Locate every blood parasite and identify its species.
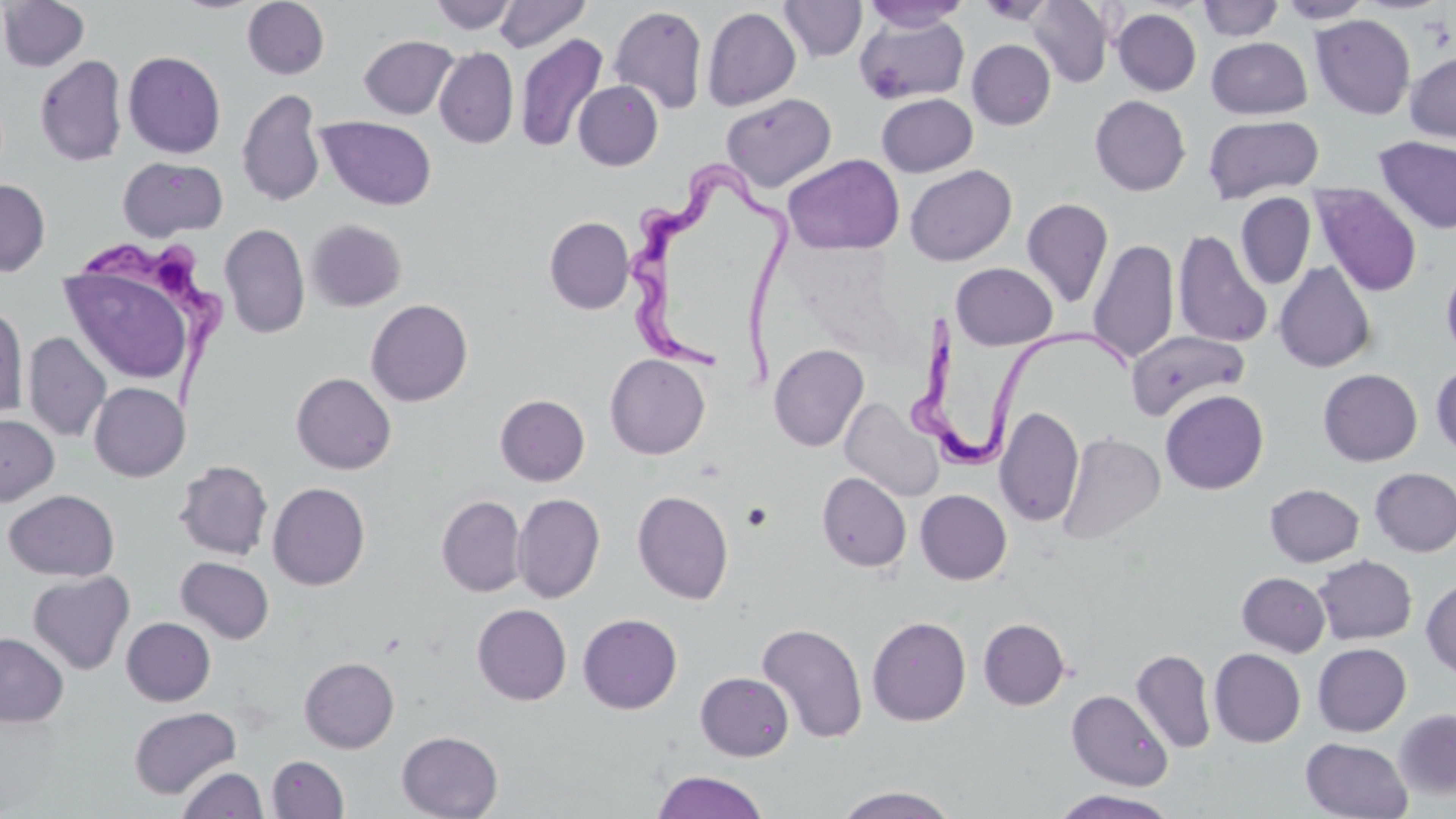
Approximate bounding boxes as (x1, y1, x2, y2) in pixels.
Trypanosoma brucei: (627, 163, 792, 391), (78, 238, 228, 414), (908, 308, 1136, 478).
No Plasmodium falciparum, Plasmodium ovale, Plasmodium malariae, Plasmodium vivax, or Babesia divergens observed.

Summary:
  - Uninfected red blood cell locations: (0, 0, 90, 72), (242, 0, 329, 79), (428, 0, 518, 35), (493, 0, 592, 52), (1027, 0, 1113, 87), (1197, 0, 1283, 42), (1277, 0, 1373, 25), (779, 1, 867, 62), (861, 1, 970, 32), (608, 5, 708, 114), (702, 7, 801, 111), (1112, 8, 1201, 96), (1310, 14, 1415, 119), (853, 15, 970, 105), (515, 34, 608, 153), (359, 35, 458, 119), (1206, 37, 1312, 119), (967, 39, 1056, 130), (435, 47, 519, 148), (123, 50, 226, 158), (1405, 51, 1456, 142), (35, 55, 127, 166), (573, 80, 663, 171), (237, 89, 326, 207), (876, 92, 978, 177), (721, 93, 836, 191), (1090, 95, 1191, 196), (1202, 114, 1324, 204), (318, 116, 436, 210), (1373, 135, 1456, 234), (783, 154, 905, 255), (118, 156, 228, 241), (905, 163, 1017, 266), (0, 179, 51, 276), (1311, 183, 1422, 297), (1235, 193, 1316, 290), (1022, 197, 1114, 309), (544, 216, 634, 314), (305, 219, 406, 312), (219, 223, 310, 339), (1172, 229, 1273, 348), (1088, 239, 1179, 365), (1441, 260, 1456, 365), (59, 261, 196, 387), (1274, 261, 1376, 372), (951, 262, 1057, 350), (366, 299, 473, 406), (0, 301, 29, 420), (1126, 329, 1251, 421), (23, 332, 111, 442), (769, 344, 869, 452), (605, 354, 710, 459), (1430, 362, 1456, 457), (1318, 368, 1422, 466), (291, 372, 396, 475), (89, 382, 188, 481), (1160, 389, 1269, 494), (495, 394, 590, 485), (839, 397, 943, 502), (995, 406, 1084, 527), (0, 414, 59, 505), (1056, 432, 1166, 545), (174, 460, 273, 560), (1370, 467, 1456, 556), (817, 472, 911, 572), (268, 482, 370, 590), (1265, 483, 1364, 566), (915, 489, 1012, 585), (3, 490, 119, 581), (632, 490, 733, 604), (513, 493, 605, 603), (436, 495, 526, 597), (1313, 555, 1417, 644), (175, 556, 274, 644), (28, 570, 134, 674), (1237, 571, 1330, 655), (1421, 577, 1456, 678), (472, 604, 571, 705), (578, 613, 682, 714), (867, 615, 971, 726), (121, 617, 215, 706), (978, 618, 1070, 710), (756, 622, 867, 743), (0, 632, 68, 727), (1312, 642, 1411, 736), (1131, 648, 1216, 754), (1209, 648, 1306, 747), (299, 657, 399, 752), (695, 672, 794, 760), (1067, 689, 1173, 790), (128, 706, 241, 799), (1393, 708, 1456, 801), (397, 731, 503, 819), (1300, 737, 1413, 819), (267, 755, 349, 819), (178, 766, 267, 819), (651, 770, 770, 819), (831, 785, 964, 819), (1051, 790, 1181, 818)
  - Slide-level diagnosis: Trypanosoma brucei
  - Stain: May-Grünwald-Giemsa
  - Magnification: 1000x
  - Field of view: single
  - Modality: optical microscopy
  - Preparation: thin blood film
  - Image size: 1456×819 pixels